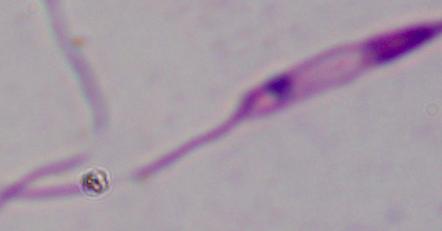
Summary:
  - Identification: Leishmania
  - Magnification: 1000x
  - Modality: micrograph